Assess the morphology of the red blood cells.
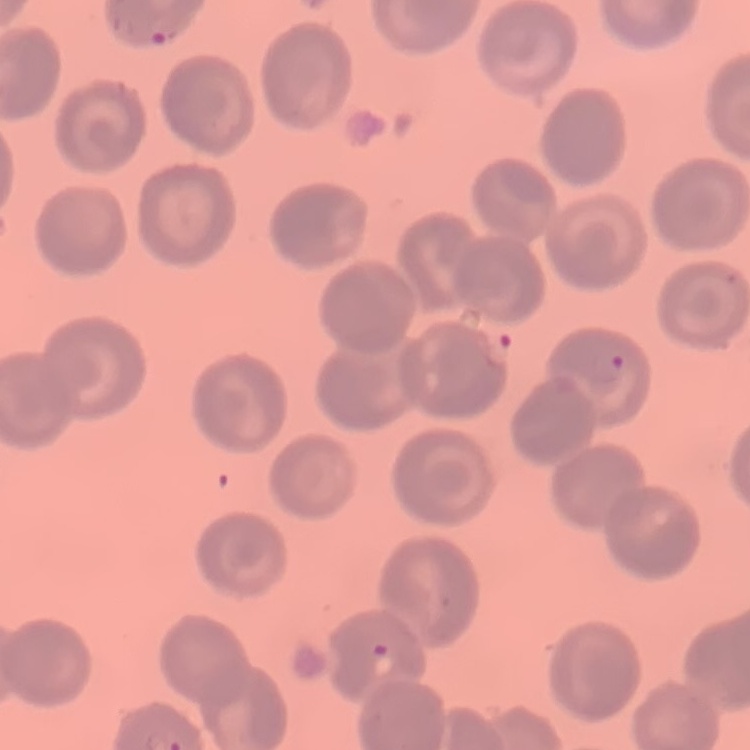
No rouleaux formation.

Thin peripheral smear. Field's or Giemsa stain. Square crop of a larger photomicrograph.